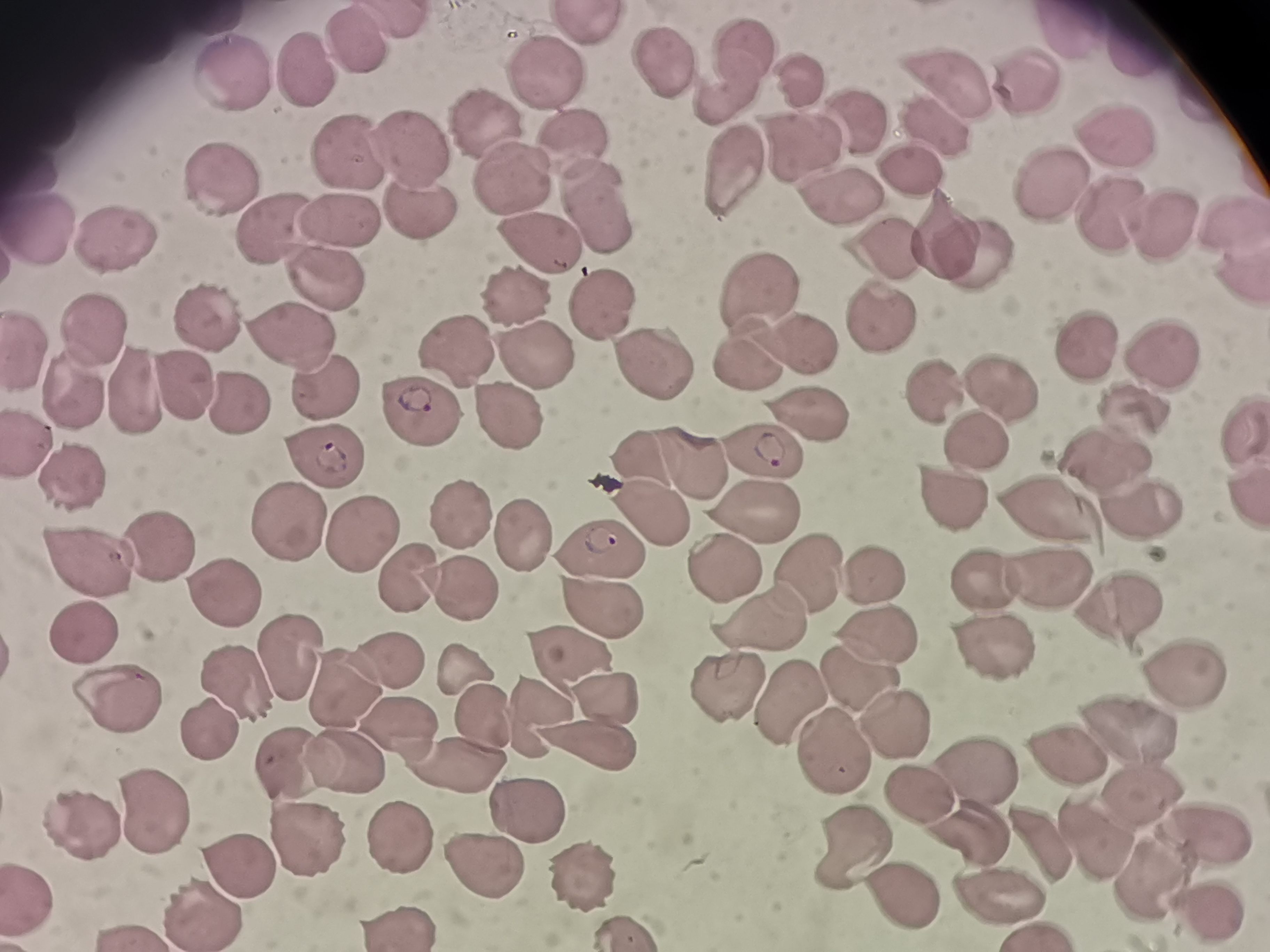
Approximate centers as [x, y] in pixels.
Summary:
  - Cell locations: [587, 28], [360, 41], [1141, 47], [732, 54], [309, 62], [666, 63], [236, 71], [546, 76], [954, 83], [1028, 86], [811, 87], [722, 91], [854, 115], [489, 117], [928, 123], [1120, 136], [412, 142], [576, 152], [808, 153], [348, 158], [911, 167], [733, 168], [222, 179], [512, 186], [1049, 188], [840, 196], [413, 202], [601, 207], [336, 217], [1115, 218], [1229, 219], [1165, 227], [45, 228], [266, 228], [120, 236], [541, 248], [949, 248], [886, 249], [971, 254], [326, 274], [1239, 277], [761, 292], [517, 299], [603, 304], [881, 314], [204, 316], [95, 323], [292, 342], [808, 342], [1082, 342], [459, 349], [30, 353], [745, 357], [1153, 357], [537, 359], [650, 363], [73, 385], [327, 388], [181, 390], [936, 391], [998, 391], [135, 392], [1141, 401], [234, 403], [504, 411], [809, 411], [420, 413], [1240, 424], [976, 437], [27, 442], [765, 450], [1113, 452], [644, 454], [325, 459], [695, 459], [74, 477], [945, 494], [1245, 494], [1055, 503], [753, 511], [651, 512], [1140, 513], [465, 519], [286, 527], [526, 532], [360, 537], [162, 546], [605, 556], [89, 565], [725, 567], [809, 572], [1047, 574], [414, 576], [874, 578], [985, 582], [458, 590], [228, 598], [600, 607], [1119, 609], [766, 616], [84, 634], [879, 636], [997, 648], [291, 656], [572, 660], [389, 661], [460, 663], [1182, 663], [854, 674], [722, 682], [240, 683], [349, 689], [789, 697], [609, 704], [117, 705], [486, 718], [891, 720], [1125, 729], [210, 731], [406, 734], [597, 746], [831, 748], [1057, 753], [347, 759], [459, 763], [970, 768], [917, 793], [1136, 797], [149, 808], [524, 811], [84, 818], [1199, 827], [398, 830], [971, 833], [300, 834], [1094, 840], [853, 843], [477, 859], [237, 867], [579, 869], [1147, 878], [903, 886], [994, 887], [1203, 905], [207, 911], [395, 923], [622, 931]
  - Field of view: single
  - Image size: 1270×952 pixels
  - Stain: Giemsa
  - Capture: smartphone camera at the microscope eyepiece
  - Preparation: thin blood smear